Report the malaria status of this cell.
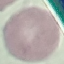
It is uninfected.

Acquired by smartphone through the microscope eyepiece. Cell patch, automatically extracted from a larger field of view and resized to 64 × 64 pixels. Giemsa stain. Thin blood film.